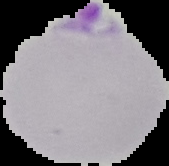
Image is 169×166 pixels. Cell region segmented out of the field of view; the surrounding area is masked to black. From a thin blood film. Result: Plasmodium parasites detected.